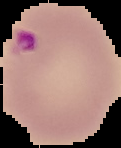

{
  "image_type": "segmented cell region with the area outside set to black",
  "preparation": "thin blood smear",
  "image_size": "121×148 pixels",
  "malaria_status": "parasitized"
}